Assess for Plasmodium parasites.
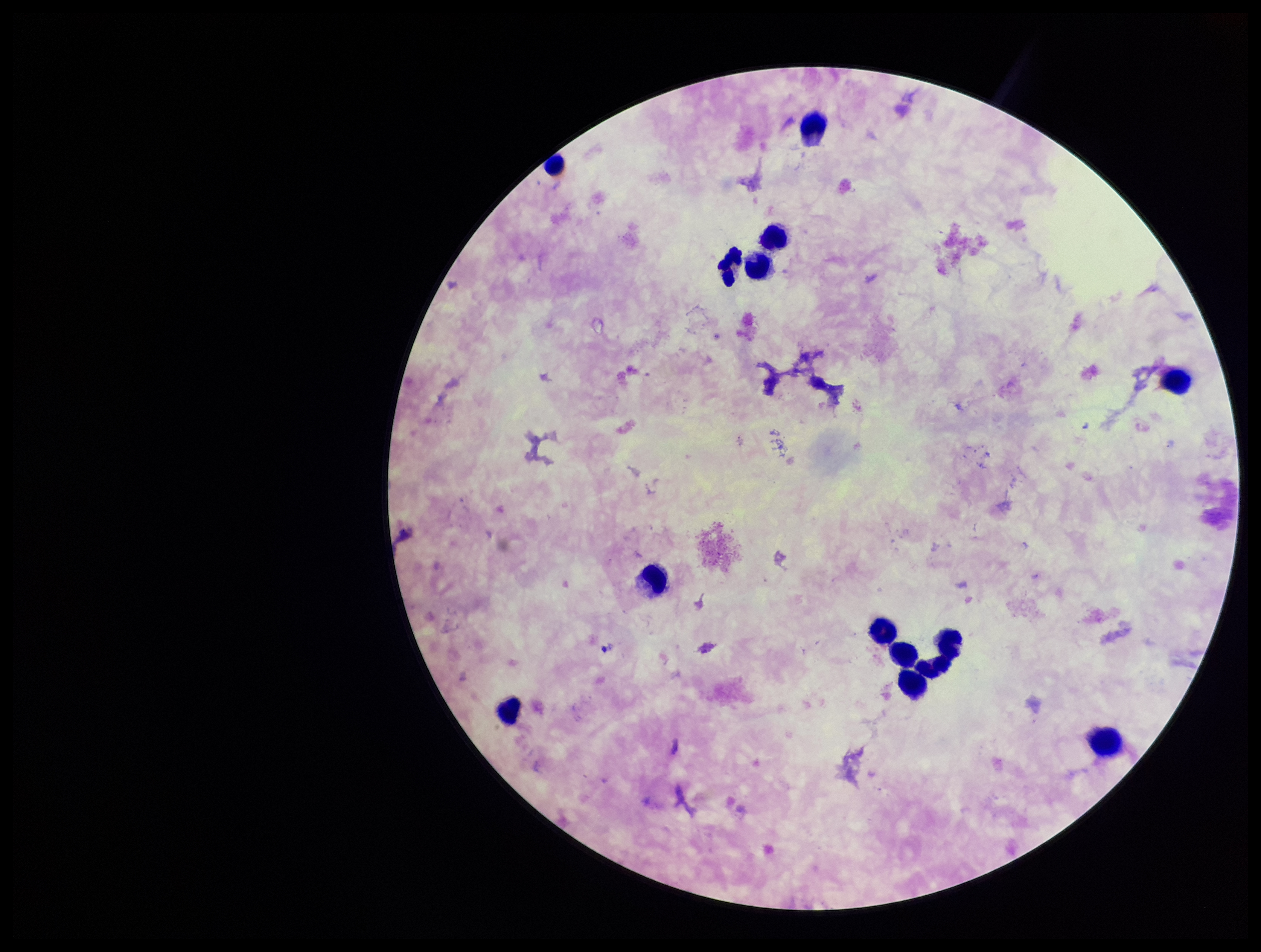

None seen.

Summary:
  - Parasite count: 0
  - Image size: 1261×952 pixels
  - Patient malaria status: infected
  - Leukocyte count: 14
  - Species reported for this patient: Plasmodium falciparum
  - Stain: Giemsa
  - Field of view: one from this slide
  - Preparation: thick
  - Capture: smartphone photograph through the microscope eyepiece